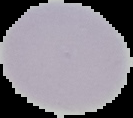 Result: no Plasmodium parasites detected. Image is 133×118 pixels. Cell region segmented out of the field of view; the surrounding area is masked to black. From a thin blood film.